Name the parasite shown.
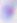

This is Toxoplasma gondii.

magnification = 400x
modality = micrograph